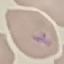
malaria_status: parasitized
image_type: cell patch, automatically extracted from a larger field of view and resized to 64 × 64 pixels
stain: Giemsa
capture: smartphone camera at the microscope eyepiece
preparation: thin blood film